Give the position of every Plasmodium parasite visible.
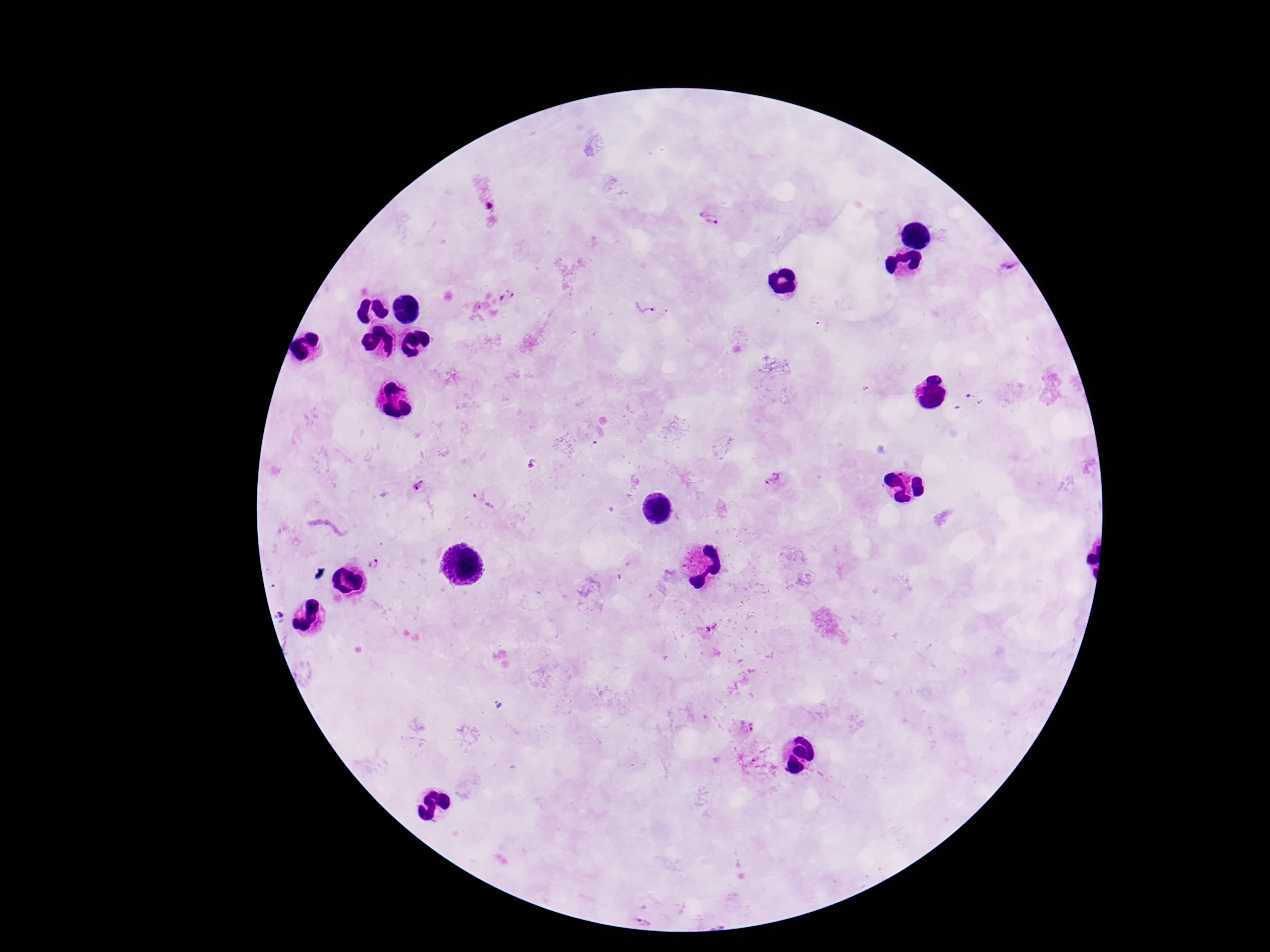

Approximate centers as [x, y] in pixels.
Plasmodium parasites: [709, 218], [1007, 267], [507, 296], [647, 303], [776, 479], [418, 484], [484, 499], [374, 564], [712, 630], [745, 728], [645, 916].

image size = 1270×952 pixels
capture = smartphone camera through the microscope eyepiece
magnification = 100x
stain = Giemsa
preparation = thick blood smear
field of view = single
patient malaria status = infected